Outline each blood parasite and name the species.
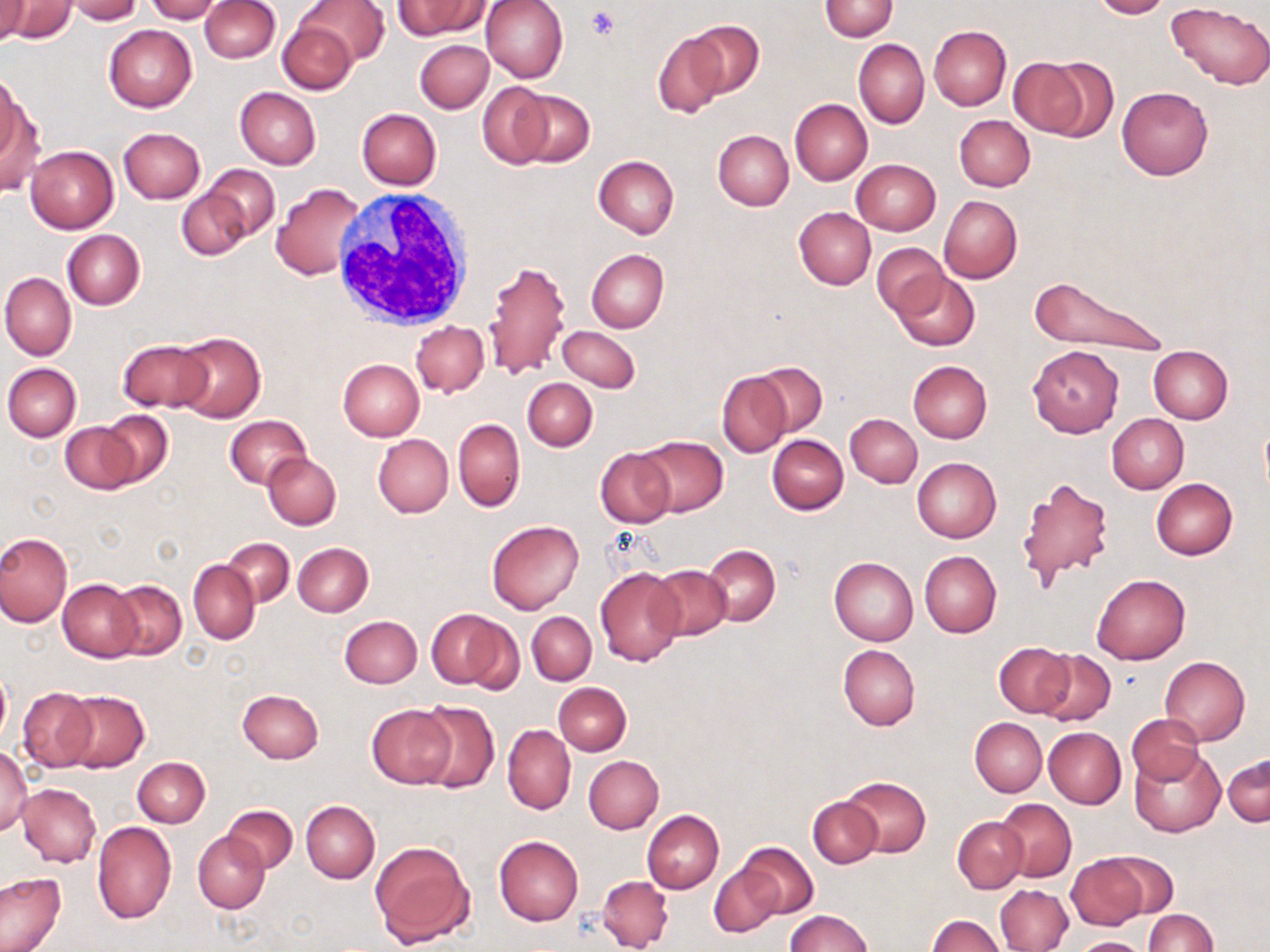

No blood parasites seen.

Approximate bounding boxes as (x1, y1, x2, y2) in pixels. Uninfected red blood cell locations: (0, 0, 31, 45), (144, 0, 222, 23), (201, 0, 279, 62), (296, 0, 389, 68), (394, 0, 489, 39), (480, 0, 569, 83), (819, 0, 898, 40), (1091, 0, 1171, 19), (1, 1, 76, 44), (64, 1, 141, 23), (1166, 2, 1270, 88), (277, 19, 359, 94), (684, 20, 764, 98), (103, 23, 197, 112), (929, 25, 1011, 110), (653, 32, 728, 119), (415, 39, 494, 113), (854, 39, 928, 128), (1019, 55, 1114, 141), (0, 79, 38, 195), (478, 82, 552, 169), (1116, 85, 1214, 180), (234, 87, 321, 170), (512, 88, 595, 166), (789, 98, 872, 186), (357, 108, 441, 189), (954, 115, 1035, 191), (118, 127, 206, 204), (713, 129, 794, 210), (24, 145, 119, 234), (593, 155, 679, 238), (851, 158, 941, 235), (204, 165, 279, 240), (270, 182, 370, 280), (177, 186, 252, 260), (939, 195, 1021, 283), (794, 208, 875, 289), (62, 229, 145, 310), (871, 243, 947, 320), (585, 248, 669, 334), (483, 257, 570, 380), (1, 271, 76, 361), (892, 271, 979, 351), (1024, 275, 1168, 357), (410, 321, 488, 397), (557, 325, 640, 393), (173, 332, 266, 422), (118, 339, 209, 412), (1027, 344, 1124, 438), (1148, 345, 1233, 423), (338, 360, 424, 441), (908, 361, 992, 443), (749, 362, 828, 438), (4, 363, 81, 442), (717, 370, 793, 459), (522, 377, 597, 450), (98, 410, 174, 489), (846, 413, 922, 487), (1106, 413, 1188, 493), (224, 415, 312, 490), (453, 417, 525, 512), (61, 422, 140, 493), (372, 433, 454, 518), (634, 434, 728, 517), (767, 434, 848, 514), (595, 447, 676, 528), (263, 451, 341, 530), (912, 458, 1001, 542), (1016, 477, 1113, 589), (1151, 479, 1238, 560), (486, 520, 583, 614), (0, 532, 72, 627), (222, 537, 294, 607), (292, 543, 373, 617), (703, 544, 781, 627), (920, 550, 1001, 637), (829, 557, 918, 646), (188, 560, 260, 644), (648, 565, 733, 641), (594, 567, 684, 665), (1092, 574, 1190, 663), (58, 579, 142, 661), (109, 580, 187, 660), (428, 609, 517, 692), (527, 611, 597, 686), (339, 615, 422, 688), (994, 641, 1075, 717), (838, 644, 920, 730), (1036, 650, 1115, 727), (1159, 655, 1249, 746), (0, 667, 11, 751), (552, 682, 632, 755), (17, 687, 97, 772), (60, 689, 150, 772), (237, 689, 324, 762), (415, 700, 500, 793), (367, 704, 454, 788), (1126, 714, 1204, 785), (970, 718, 1047, 796), (503, 724, 575, 814), (1043, 726, 1126, 809), (0, 746, 33, 834), (1130, 747, 1225, 836), (1223, 753, 1269, 826), (583, 755, 663, 833), (133, 756, 209, 826), (839, 776, 931, 858), (17, 784, 102, 866), (807, 796, 883, 868), (995, 798, 1077, 882), (301, 800, 380, 883), (222, 805, 297, 873), (643, 810, 725, 894), (952, 816, 1028, 892), (91, 821, 176, 924), (193, 830, 270, 913), (494, 836, 584, 926), (370, 840, 474, 947), (735, 842, 818, 918), (1096, 851, 1177, 922), (1066, 855, 1146, 930), (709, 862, 785, 938), (0, 873, 68, 952), (597, 875, 674, 952), (996, 884, 1072, 952), (1143, 909, 1216, 951), (787, 910, 871, 952), (927, 915, 1004, 952), (1068, 937, 1148, 952). Platelet locations: (586, 7, 620, 39). White blood cell locations: (329, 192, 476, 331). Slide-level diagnosis: no evidence of blood parasites. Single field of view. Image is 1270×952 pixels. Optical microscopy. Thin blood smear. Captured at 1000x magnification. May-Grünwald-Giemsa stain.